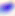
Summary:
  - Identification: Toxoplasma gondii
  - Magnification: 400x
  - Modality: photomicrograph